Locate every blood parasite and identify its species.
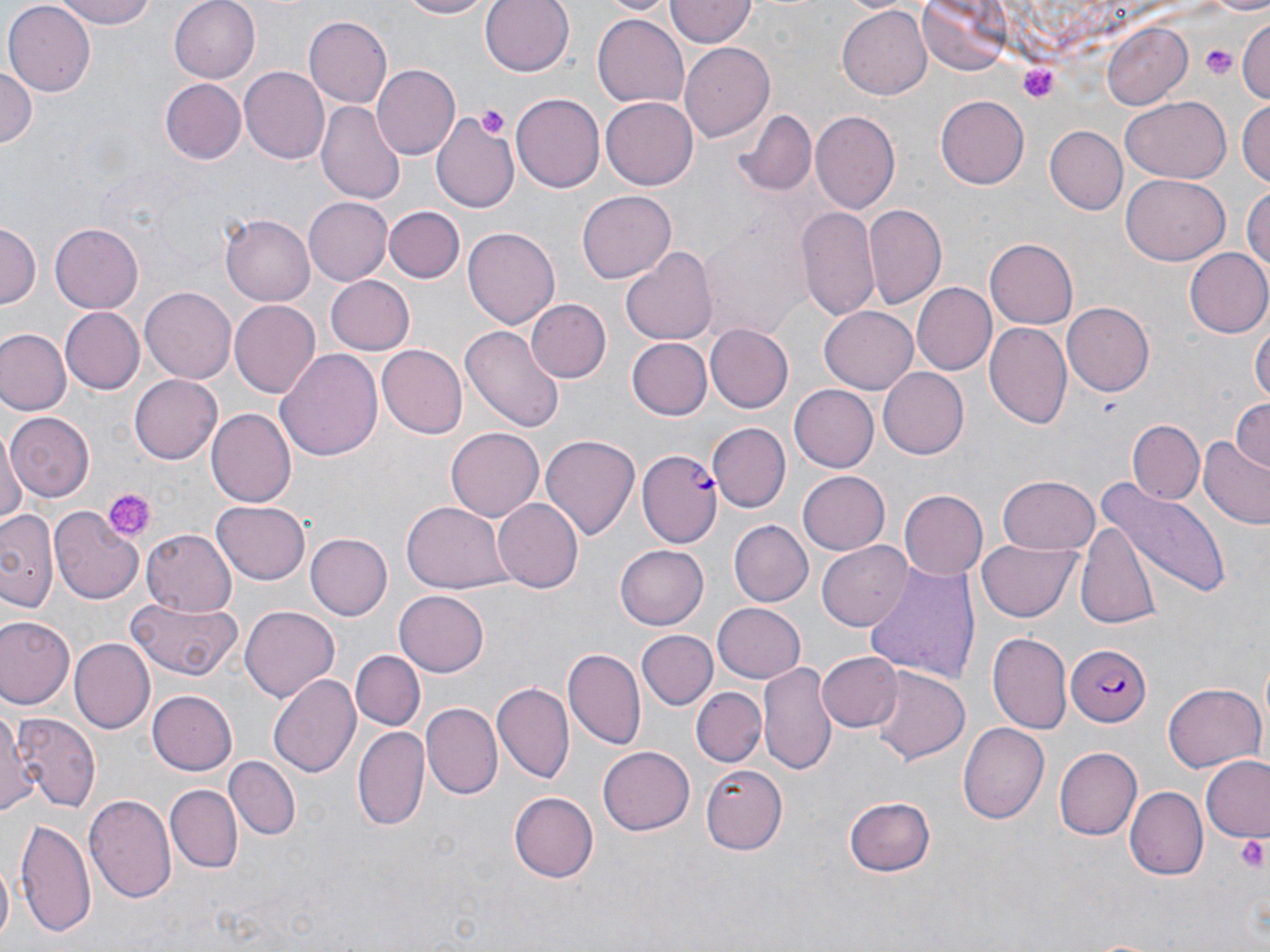

Approximate bounding boxes as (x1,y1)-(x2,y2) corner pairs in pixels.
Plasmodium falciparum-infected red blood cells: (637,450)-(722,546), (1064,642)-(1151,725).
No Plasmodium ovale, Plasmodium malariae, Plasmodium vivax, Babesia divergens, or Trypanosoma brucei observed.

Summary:
  - Uninfected red blood cell locations: (49,0)-(164,28), (168,0)-(261,83), (393,0)-(493,20), (481,0)-(575,76), (602,0)-(679,17), (917,0)-(1013,77), (3,2)-(95,96), (665,2)-(755,47), (837,4)-(933,98), (592,12)-(689,107), (301,16)-(393,109), (1235,17)-(1270,107), (1103,22)-(1194,109), (678,42)-(777,143), (0,63)-(37,155), (240,65)-(333,163), (373,65)-(458,158), (159,78)-(245,165), (511,94)-(605,191), (1121,96)-(1231,182), (936,97)-(1029,188), (601,98)-(697,189), (1236,99)-(1270,188), (316,100)-(405,206), (735,109)-(815,197), (431,111)-(524,212), (809,112)-(901,213), (1043,125)-(1128,215), (1121,174)-(1230,266), (1243,185)-(1270,281), (578,189)-(675,281), (305,198)-(391,284), (863,204)-(945,309), (386,206)-(464,282), (798,207)-(881,322), (223,211)-(318,306), (1,222)-(39,311), (51,223)-(144,312), (702,223)-(803,331), (465,228)-(559,327), (986,240)-(1080,329), (622,246)-(717,344), (1183,248)-(1270,339), (327,276)-(414,356), (914,282)-(999,374), (139,287)-(237,383), (229,298)-(320,395), (524,299)-(609,383), (1061,301)-(1155,396), (59,307)-(144,393), (821,307)-(917,393), (1252,319)-(1269,410), (984,322)-(1071,431), (705,324)-(794,413), (461,325)-(565,436), (0,330)-(68,416), (627,338)-(711,420), (376,345)-(467,438), (275,347)-(383,464), (878,368)-(969,459), (128,374)-(222,465), (788,384)-(877,471), (1230,399)-(1270,472), (206,410)-(295,508), (6,412)-(93,501), (1128,420)-(1204,504), (711,423)-(790,513), (446,428)-(546,523), (0,433)-(24,529), (541,433)-(640,543), (1198,436)-(1270,529), (798,469)-(891,554), (1095,473)-(1229,594), (995,476)-(1101,556), (898,491)-(987,581), (492,497)-(584,591), (211,500)-(312,584), (402,502)-(511,595), (0,510)-(59,611), (51,510)-(143,605), (1075,517)-(1163,632), (728,520)-(811,607), (141,527)-(238,615), (304,532)-(391,620), (979,538)-(1084,622), (614,541)-(708,628), (817,541)-(913,631), (863,561)-(982,686), (394,591)-(489,676), (127,595)-(244,680), (711,603)-(806,683), (241,605)-(340,701), (1,613)-(75,710), (638,631)-(715,709), (988,633)-(1070,734), (71,640)-(153,735), (564,647)-(645,750), (353,650)-(424,729), (819,651)-(901,732), (760,660)-(835,773), (870,667)-(971,766), (267,673)-(361,780), (1162,682)-(1265,773), (489,684)-(574,784), (692,685)-(766,768), (149,692)-(237,775), (2,698)-(24,818), (423,703)-(502,799), (11,714)-(99,810), (960,723)-(1049,824), (352,724)-(431,829), (598,746)-(694,836), (1055,747)-(1142,839), (223,756)-(301,841), (1199,757)-(1270,841), (696,766)-(787,855), (166,785)-(242,871), (1125,787)-(1207,880), (508,792)-(597,882), (85,793)-(176,904), (843,795)-(936,878), (14,817)-(97,936), (1,862)-(13,946)
  - Platelet locations: (1200,43)-(1238,78), (1018,64)-(1060,107), (478,104)-(509,137), (104,490)-(154,540), (1235,833)-(1269,876)
  - Slide-level diagnosis: Plasmodium falciparum
  - Field of view: single
  - Preparation: thin blood film
  - Stain: May-Grünwald-Giemsa
  - Magnification: 1000x
  - Image size: 1270×952 pixels
  - Modality: light microscopy